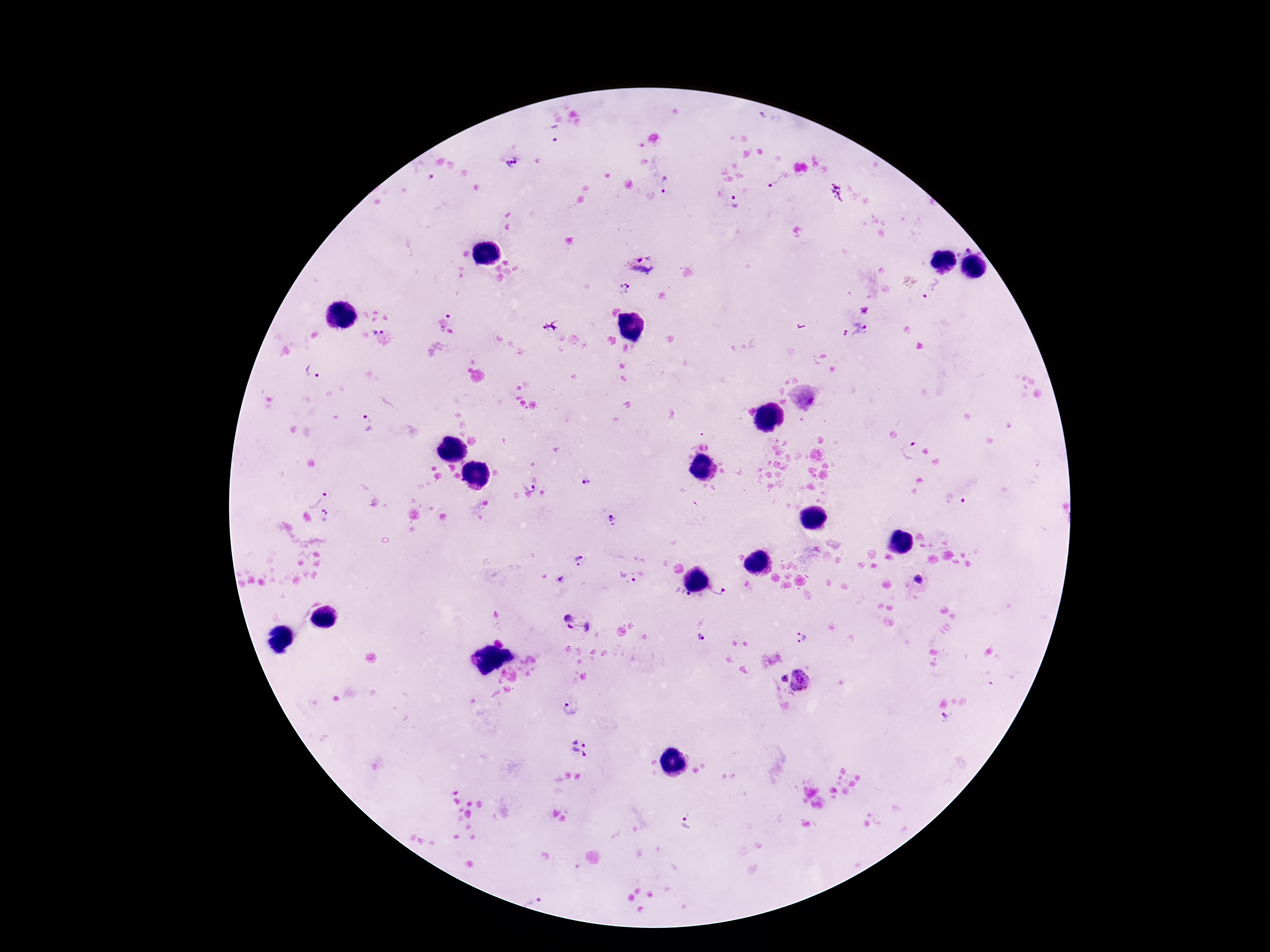
Approximate centers as (x, y) in pixels. Plasmodium parasite locations: (555, 132), (512, 163), (424, 173), (776, 181), (666, 187), (837, 193), (735, 200), (968, 249), (642, 265), (624, 288), (932, 290), (864, 308), (453, 319), (854, 330), (377, 331), (313, 371), (369, 424), (908, 453), (585, 482), (530, 487), (315, 498), (953, 501), (327, 516), (613, 520), (581, 560), (627, 579), (920, 579), (561, 580), (719, 593), (577, 622), (701, 637), (801, 638), (783, 678), (800, 680), (571, 710), (944, 718), (580, 747), (688, 824). Image is 1270×952 pixels. One field from this slide. Photographed through the microscope eyepiece with a smartphone camera. Patient malaria status: positive. 100x magnification. Giemsa stain. Thick peripheral-blood smear.